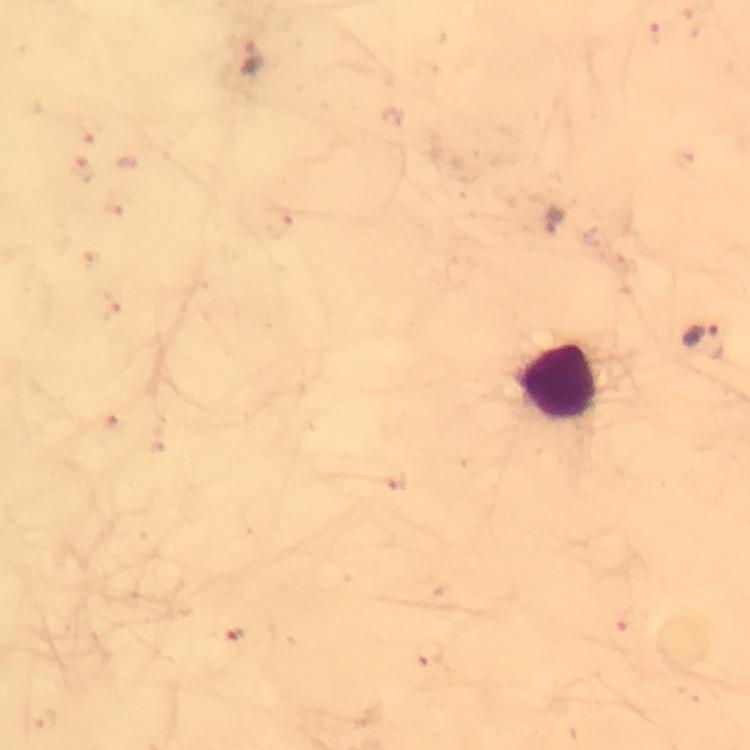
Approximate centers as [x, y] in pixels.
Summary:
  - Malaria parasite locations: [251, 56], [707, 341]
  - Leukocyte locations: [560, 381]
  - Immersion oil: applied
  - Image size: 750×750 pixels
  - Capture: smartphone mounted on the microscope
  - Preparation: thick blood film
  - Context: from a malaria diagnostic workup
  - Cropped from: one field of view
  - Stain: Giemsa
  - Magnification: 100x